Assess this cell for malaria.
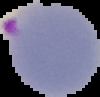

It is parasitized.

Summary:
  - Image size: 100×97 pixels
  - Preparation: thin blood smear
  - Image type: cell region segmented out of the field of view; surrounding area masked to black